Report the malaria status of this cell.
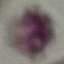
Uninfected.

Giemsa-stained preparation. Thin smear of blood. Photographed with a smartphone camera at the microscope eyepiece. Cell patch, automatically extracted from a larger field of view and resized to 64 × 64 pixels.